Classify this cell by malaria status.
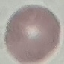
It is uninfected.

stain = Giemsa
image type = cell patch, automatically extracted from a larger field of view and resized to 64 × 64 pixels
capture = smartphone through the microscope eyepiece
preparation = thin blood film